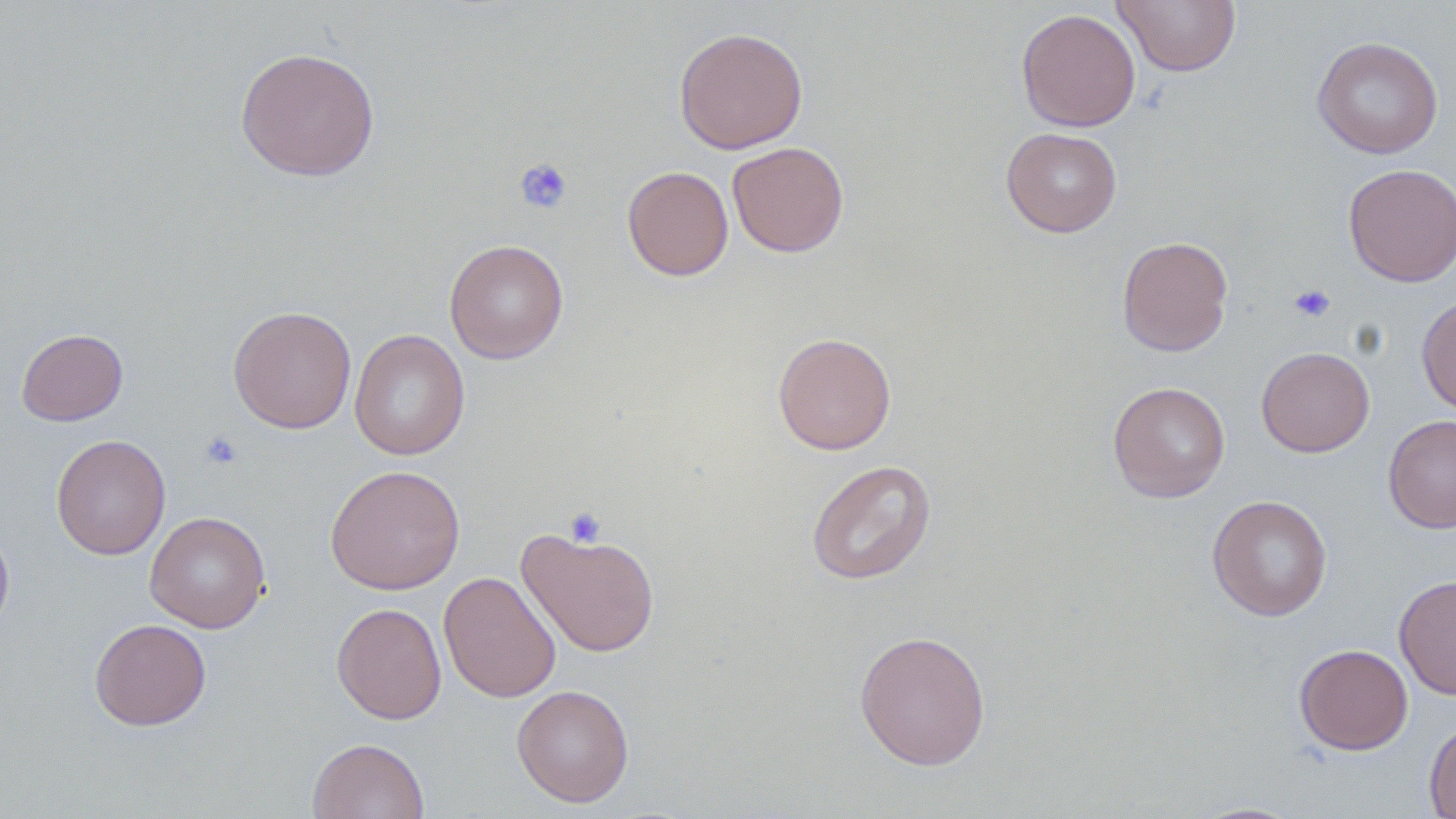

Summary:
  - Coordinate format: approximate bounding boxes as (x1, y1, x2, y2) in pixels
  - Platelet locations: (514, 158, 573, 214), (1288, 284, 1335, 323), (200, 430, 243, 469), (562, 508, 606, 546)
  - Uninfected red blood cell locations: (1112, 1, 1242, 76), (1016, 7, 1141, 132), (673, 27, 809, 154), (1312, 36, 1443, 159), (235, 46, 380, 182), (1001, 127, 1122, 238), (727, 141, 849, 258), (1343, 163, 1456, 287), (622, 165, 734, 281), (1116, 236, 1233, 357), (444, 239, 569, 364), (1416, 294, 1456, 416), (228, 305, 357, 434), (16, 328, 128, 426), (349, 328, 470, 460), (772, 332, 896, 455), (1256, 347, 1375, 457), (1107, 381, 1231, 503), (1383, 413, 1456, 534), (51, 434, 171, 560), (806, 459, 936, 585), (324, 464, 465, 595), (1207, 494, 1333, 621), (145, 511, 271, 633), (0, 523, 14, 637), (517, 526, 661, 658), (439, 571, 561, 703), (1394, 574, 1456, 699), (332, 602, 447, 724), (88, 618, 212, 731), (854, 629, 992, 771), (1294, 643, 1413, 755), (511, 684, 635, 807), (1423, 720, 1456, 819), (307, 737, 430, 819), (1188, 801, 1307, 818)
  - Slide-level diagnosis: no evidence of blood parasites
  - Preparation: thin blood film
  - Stain: May-Grünwald-Giemsa
  - Modality: light microscopy
  - Field of view: one of a larger specimen
  - Magnification: 1000x
  - Image size: 1456×819 pixels